Locate every Plasmodium vivax-infected red blood cell.
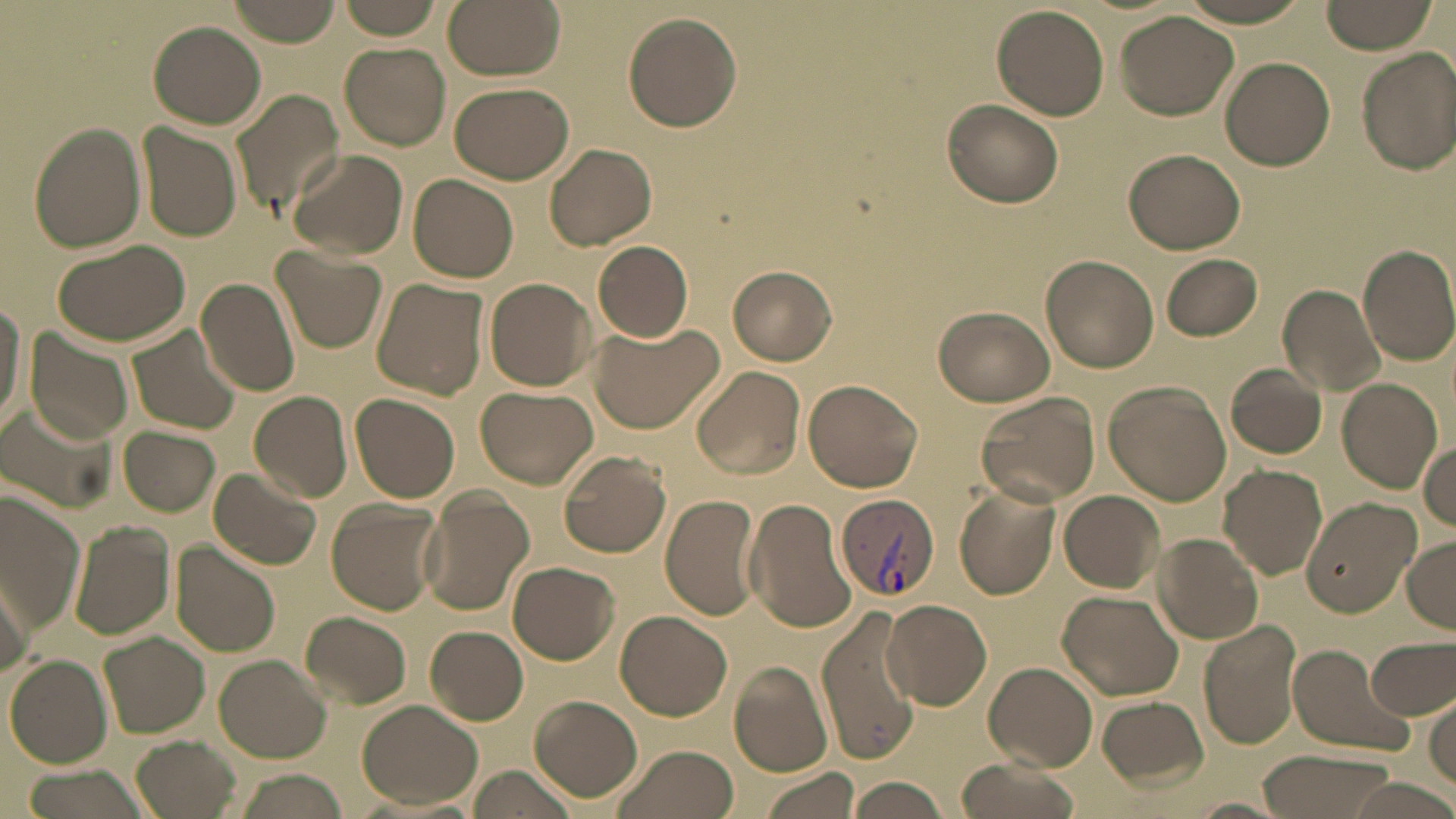

Approximate bounding boxes as [x1, y1, x2, y2] in pixels.
Plasmodium vivax-infected red blood cells: [834, 492, 940, 605].

slide-level diagnosis = Plasmodium vivax
uninfected red blood cell locations = approximate bounding boxes as [x1, y1, x2, y2] in pixels: [228, 0, 342, 46], [335, 0, 448, 39], [441, 0, 565, 79], [1318, 0, 1436, 55], [992, 5, 1109, 120], [1115, 11, 1242, 121], [624, 13, 741, 132], [148, 22, 266, 129], [340, 42, 451, 149], [1357, 46, 1456, 175], [1219, 57, 1335, 171], [449, 82, 574, 184], [231, 87, 345, 220], [941, 100, 1064, 209], [26, 122, 147, 254], [137, 125, 242, 242], [545, 143, 657, 251], [1124, 147, 1245, 255], [290, 150, 408, 259], [409, 174, 519, 283], [53, 238, 191, 347], [592, 240, 695, 340], [1357, 244, 1456, 366], [274, 248, 387, 354], [1041, 254, 1156, 372], [1159, 254, 1263, 341], [726, 264, 836, 366], [195, 277, 301, 399], [370, 277, 488, 401], [483, 277, 596, 391], [1278, 286, 1385, 397], [0, 293, 27, 437], [933, 306, 1057, 407], [589, 321, 725, 435], [126, 325, 242, 437], [26, 328, 135, 445], [692, 364, 806, 478], [1225, 364, 1327, 460], [802, 378, 924, 493], [1337, 379, 1442, 492], [1102, 381, 1231, 505], [477, 387, 597, 488], [249, 390, 352, 504], [973, 391, 1099, 507], [351, 393, 460, 504], [6, 397, 123, 509], [954, 412, 1080, 571], [119, 426, 219, 515], [1420, 440, 1456, 534], [558, 451, 671, 558], [1219, 465, 1328, 579], [206, 467, 322, 571], [953, 485, 1061, 599], [0, 487, 83, 632], [416, 488, 533, 615], [1058, 490, 1165, 593], [660, 494, 761, 620], [1300, 495, 1419, 618], [743, 497, 859, 635], [326, 498, 443, 617], [68, 521, 175, 640], [1152, 532, 1262, 646], [1404, 534, 1456, 632], [170, 540, 280, 659], [509, 561, 620, 663], [0, 568, 33, 677], [1057, 591, 1185, 701], [882, 599, 991, 710], [816, 606, 922, 766], [301, 611, 412, 709], [616, 611, 732, 721], [1199, 620, 1303, 748], [427, 627, 529, 723], [100, 631, 211, 738], [1366, 635, 1456, 720], [1284, 642, 1416, 757], [6, 654, 113, 768], [214, 654, 330, 763], [729, 661, 833, 775], [985, 661, 1098, 769], [1427, 691, 1456, 794], [528, 695, 642, 803], [1098, 696, 1208, 792], [357, 699, 482, 809], [129, 734, 238, 818], [612, 744, 740, 819], [1254, 748, 1399, 818], [953, 755, 1084, 819], [466, 765, 579, 818], [19, 767, 154, 819], [756, 767, 863, 818], [232, 770, 345, 819], [846, 777, 952, 817], [1338, 777, 1456, 818], [1188, 796, 1290, 817]
modality = light microscopy
magnification = 1000x
image size = 1456×819 pixels
preparation = thin blood smear
field of view = one of a larger specimen
stain = May-Grünwald-Giemsa